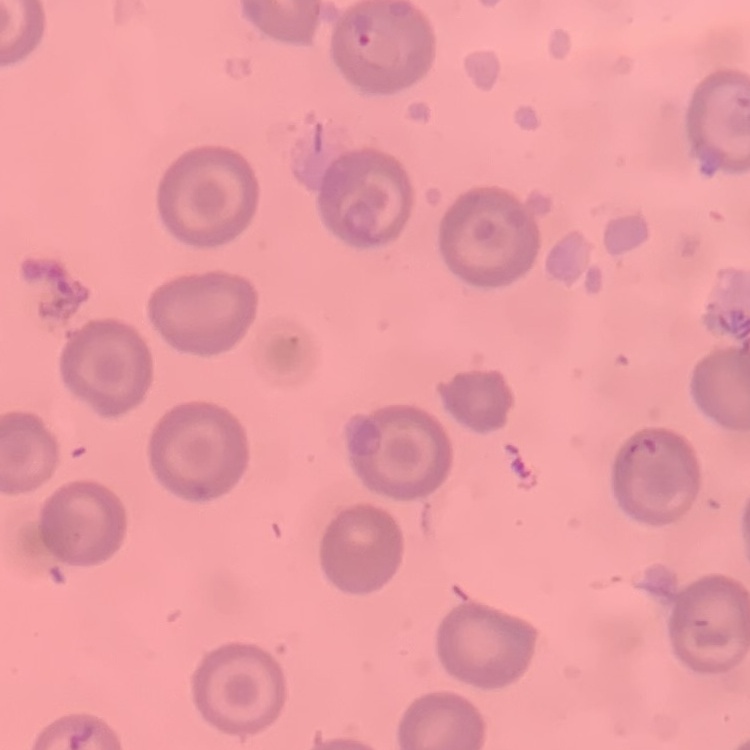

Summary:
  - Red blood cell morphology: no rouleaux formation
  - Preparation: thin blood smear
  - Stain: Field's or Giemsa
  - Image type: one tile cut from a larger photomicrograph